Report the malaria status of this cell.
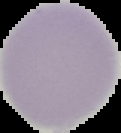

It is uninfected.

Summary:
  - Preparation: thin blood smear
  - Image size: 121×133 pixels
  - Image type: cell region segmented out of the field of view; surrounding area masked to black